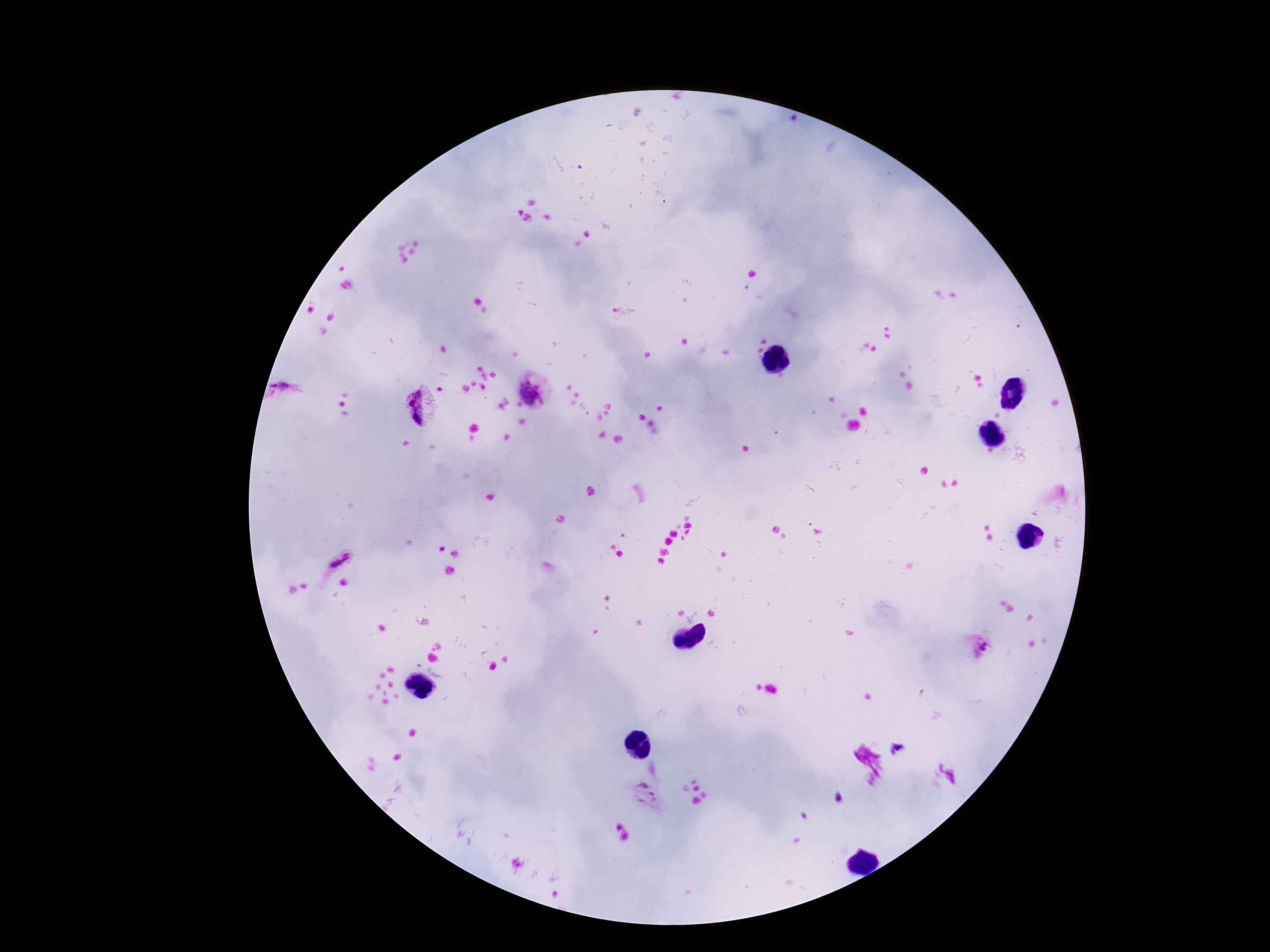

Plasmodium parasite locations = approximate centers as (x, y) in pixels: (287, 391), (529, 391), (420, 407), (340, 562), (981, 647), (643, 796)
field of view = single
patient malaria status = positive
magnification = 100x
preparation = thick peripheral-blood smear
stain = Giemsa
image size = 1270×952 pixels
capture = smartphone camera through the microscope eyepiece